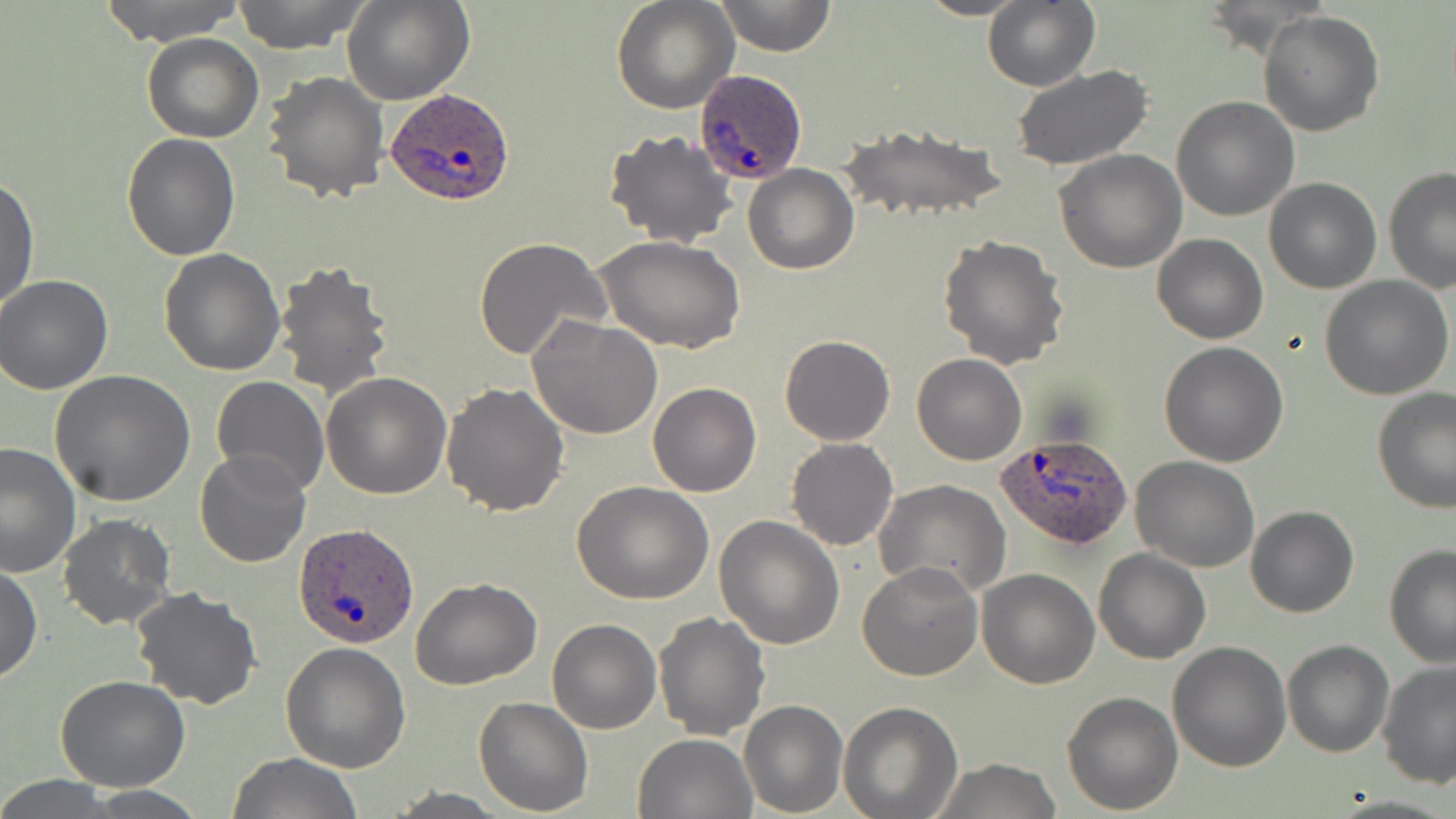

slide_level_diagnosis: Plasmodium ovale
preparation: thin blood film
image_size: 1456×819 pixels
modality: light microscopy
stain: May-Grünwald-Giemsa
uninfected_red_blood_cell_locations: 'approximate bounding boxes as named x1/y1/x2/y2 corners in pixels: (x1=95, y1=0, x2=247, y2=46), (x1=231, y1=0, x2=371, y2=53), (x1=344, y1=0, x2=474, y2=105), (x1=612, y1=0, x2=739, y2=113), (x1=714, y1=0, x2=837, y2=57), (x1=913, y1=0, x2=1032, y2=20), (x1=983, y1=1, x2=1099, y2=90), (x1=1259, y1=10, x2=1384, y2=137), (x1=142, y1=33, x2=265, y2=143), (x1=1010, y1=66, x2=1153, y2=168), (x1=264, y1=71, x2=389, y2=203), (x1=1171, y1=96, x2=1300, y2=221), (x1=840, y1=122, x2=1006, y2=225), (x1=604, y1=130, x2=738, y2=248), (x1=121, y1=132, x2=241, y2=260), (x1=1054, y1=150, x2=1187, y2=274), (x1=742, y1=166, x2=859, y2=274), (x1=1383, y1=166, x2=1456, y2=294), (x1=1, y1=175, x2=38, y2=313), (x1=1264, y1=176, x2=1381, y2=292), (x1=1153, y1=234, x2=1267, y2=343), (x1=939, y1=236, x2=1069, y2=369), (x1=475, y1=237, x2=611, y2=360), (x1=599, y1=237, x2=744, y2=354), (x1=158, y1=248, x2=287, y2=375), (x1=273, y1=261, x2=397, y2=400), (x1=1321, y1=274, x2=1453, y2=399), (x1=0, y1=275, x2=113, y2=395), (x1=528, y1=315, x2=663, y2=440), (x1=780, y1=334, x2=895, y2=446), (x1=1159, y1=341, x2=1290, y2=466), (x1=912, y1=353, x2=1027, y2=465), (x1=51, y1=370, x2=194, y2=506), (x1=322, y1=370, x2=452, y2=498), (x1=210, y1=376, x2=328, y2=496), (x1=440, y1=382, x2=569, y2=518), (x1=648, y1=383, x2=761, y2=497), (x1=1372, y1=390, x2=1456, y2=514), (x1=786, y1=438, x2=897, y2=551), (x1=0, y1=440, x2=81, y2=580), (x1=193, y1=449, x2=311, y2=569), (x1=1130, y1=455, x2=1259, y2=572), (x1=874, y1=480, x2=1011, y2=599), (x1=573, y1=481, x2=713, y2=604), (x1=1246, y1=505, x2=1360, y2=618), (x1=56, y1=512, x2=178, y2=630), (x1=714, y1=515, x2=844, y2=648), (x1=1382, y1=543, x2=1456, y2=667), (x1=1093, y1=548, x2=1211, y2=664), (x1=1, y1=562, x2=42, y2=683), (x1=857, y1=562, x2=982, y2=681), (x1=977, y1=568, x2=1098, y2=688), (x1=411, y1=575, x2=542, y2=689), (x1=129, y1=586, x2=262, y2=711), (x1=653, y1=611, x2=771, y2=740), (x1=547, y1=619, x2=662, y2=734), (x1=1282, y1=639, x2=1394, y2=758), (x1=280, y1=641, x2=411, y2=773), (x1=1168, y1=642, x2=1293, y2=772), (x1=1375, y1=661, x2=1456, y2=788), (x1=55, y1=676, x2=189, y2=792), (x1=1062, y1=689, x2=1184, y2=812), (x1=474, y1=696, x2=594, y2=816), (x1=739, y1=700, x2=849, y2=817), (x1=839, y1=702, x2=964, y2=818), (x1=632, y1=731, x2=757, y2=819), (x1=225, y1=752, x2=365, y2=819), (x1=928, y1=758, x2=1064, y2=818), (x1=0, y1=775, x2=120, y2=818), (x1=382, y1=788, x2=509, y2=817)'
plasmodium_ovale_infected_red_blood_cell_locations: 'approximate bounding boxes as named x1/y1/x2/y2 corners in pixels: (x1=695, y1=70, x2=809, y2=185), (x1=386, y1=87, x2=515, y2=207), (x1=997, y1=433, x2=1133, y2=550), (x1=294, y1=521, x2=418, y2=647)'
magnification: 1000x
field_of_view: single